State the blood parasite species.
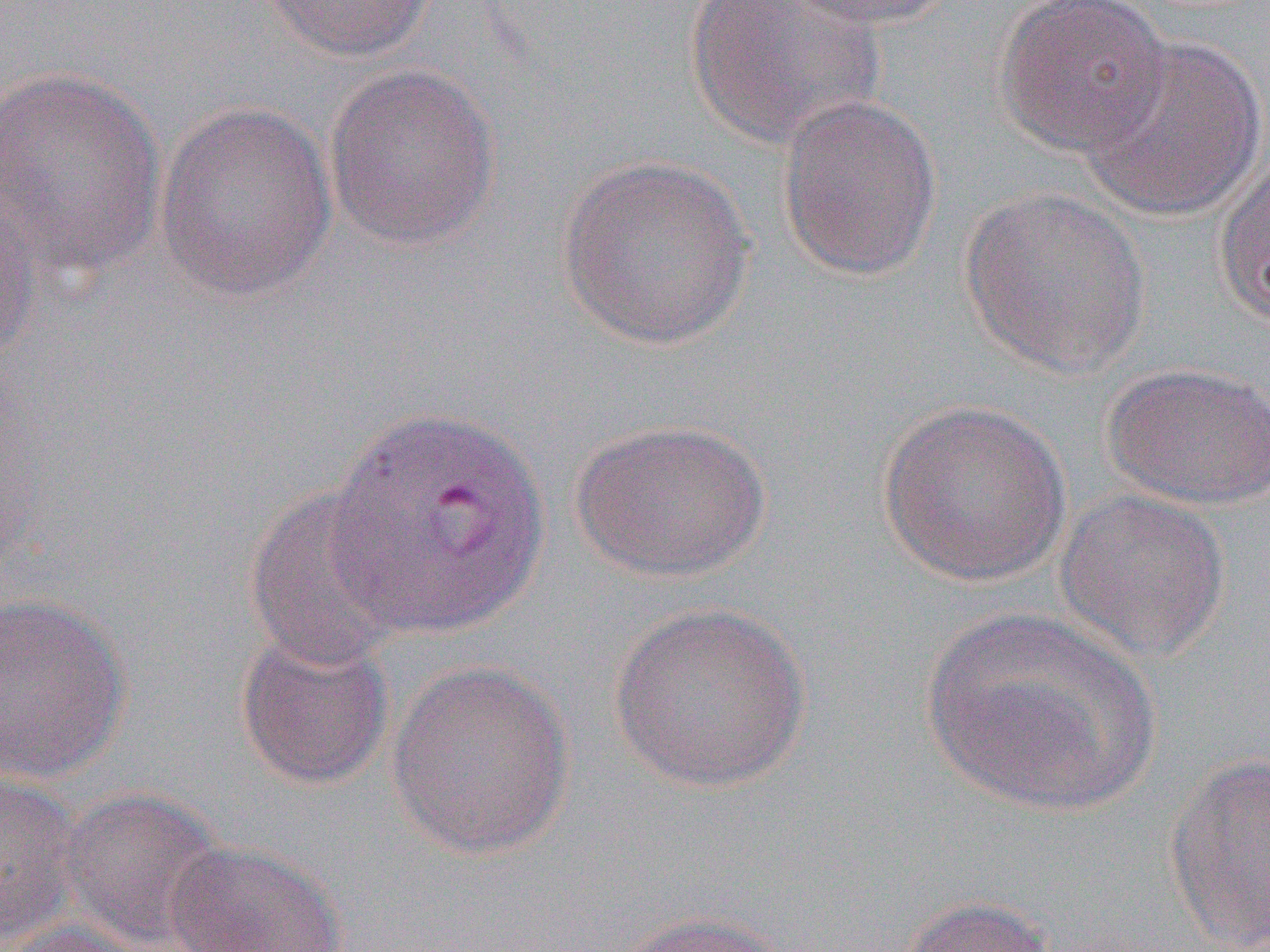

Plasmodium vivax.

Approximate bounding boxes as [x1, y1, x2, y2] in pixels. Uninfected red blood cell locations: [684, 0, 886, 149], [777, 0, 962, 31], [994, 0, 1172, 157], [255, 1, 438, 63], [1077, 32, 1267, 222], [323, 62, 502, 251], [1, 66, 168, 278], [776, 94, 943, 283], [154, 99, 338, 303], [556, 153, 757, 351], [1215, 158, 1270, 330], [958, 186, 1152, 378], [0, 188, 40, 362], [1101, 361, 1270, 510], [1, 368, 47, 573], [877, 398, 1072, 588], [569, 417, 773, 583], [243, 485, 414, 672], [1055, 488, 1232, 662], [0, 590, 133, 784], [608, 601, 812, 792], [920, 608, 1160, 814], [234, 625, 396, 791], [386, 659, 576, 860], [1163, 749, 1270, 951], [0, 769, 82, 949], [57, 786, 229, 949], [164, 839, 350, 952], [892, 895, 1060, 951], [613, 909, 799, 952], [3, 920, 163, 952]. Plasmodium vivax-infected red blood cell locations: [325, 404, 552, 640]. Image is 1270×952 pixels. 1000x magnification. Thin blood film. Optical microscopy. One field of a larger specimen.